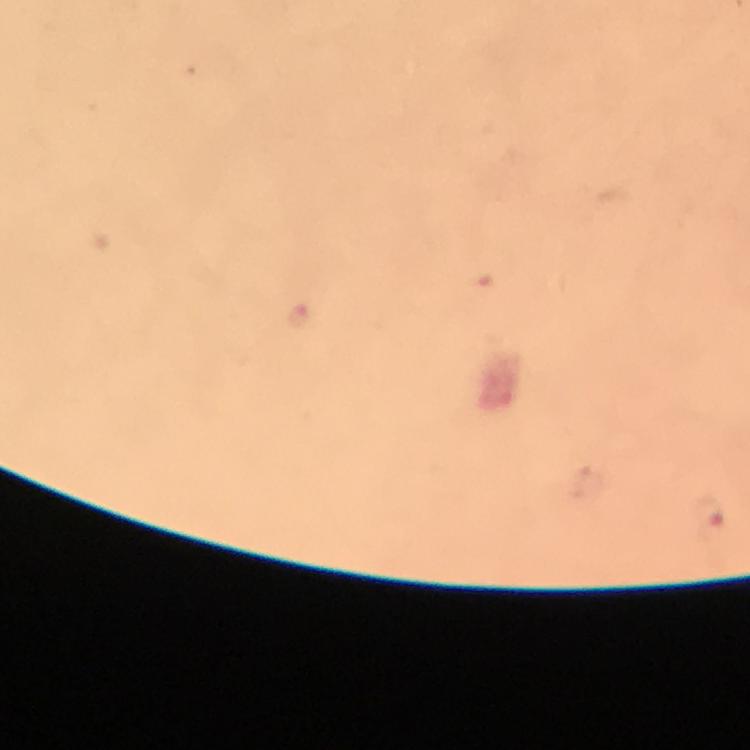
capture = smartphone photograph through a microscope
image size = 750×750 pixels
cropped from = a single field of view
context = from a diagnostic examination for malaria
Plasmodium parasite locations = approximate centers as [x, y] in pixels: [298, 318], [710, 514]
immersion oil = applied
stain = Giemsa
preparation = thick smear
magnification = 100x